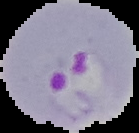 Malaria status: parasitized. Cell region segmented out of the field of view; the surrounding area is masked to black. Image is 139×133 pixels. From a thin blood film.